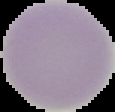

Summary:
  - Result: no Plasmodium parasites seen
  - Image size: 115×112 pixels
  - Preparation: thin blood smear
  - Image type: cell region segmented out of the field of view; surrounding area masked to black